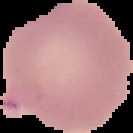
image size = 133×133 pixels
preparation = thin blood film
result = no malaria parasites seen
image type = segmented cell region with the area outside set to black